Name the parasite shown.
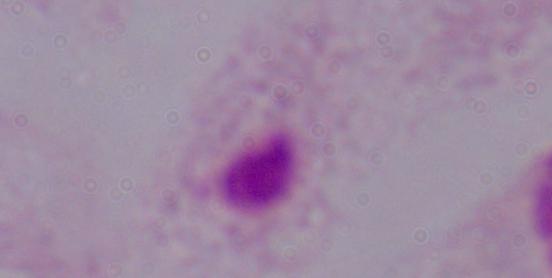
A trichomonad.

magnification = 1000x
modality = micrograph